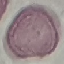
Summary:
  - Malaria status: uninfected
  - Image type: automatically extracted cell patch, resized to 64 × 64 pixels
  - Preparation: thin blood film
  - Stain: Giemsa
  - Capture: smartphone through the microscope eyepiece